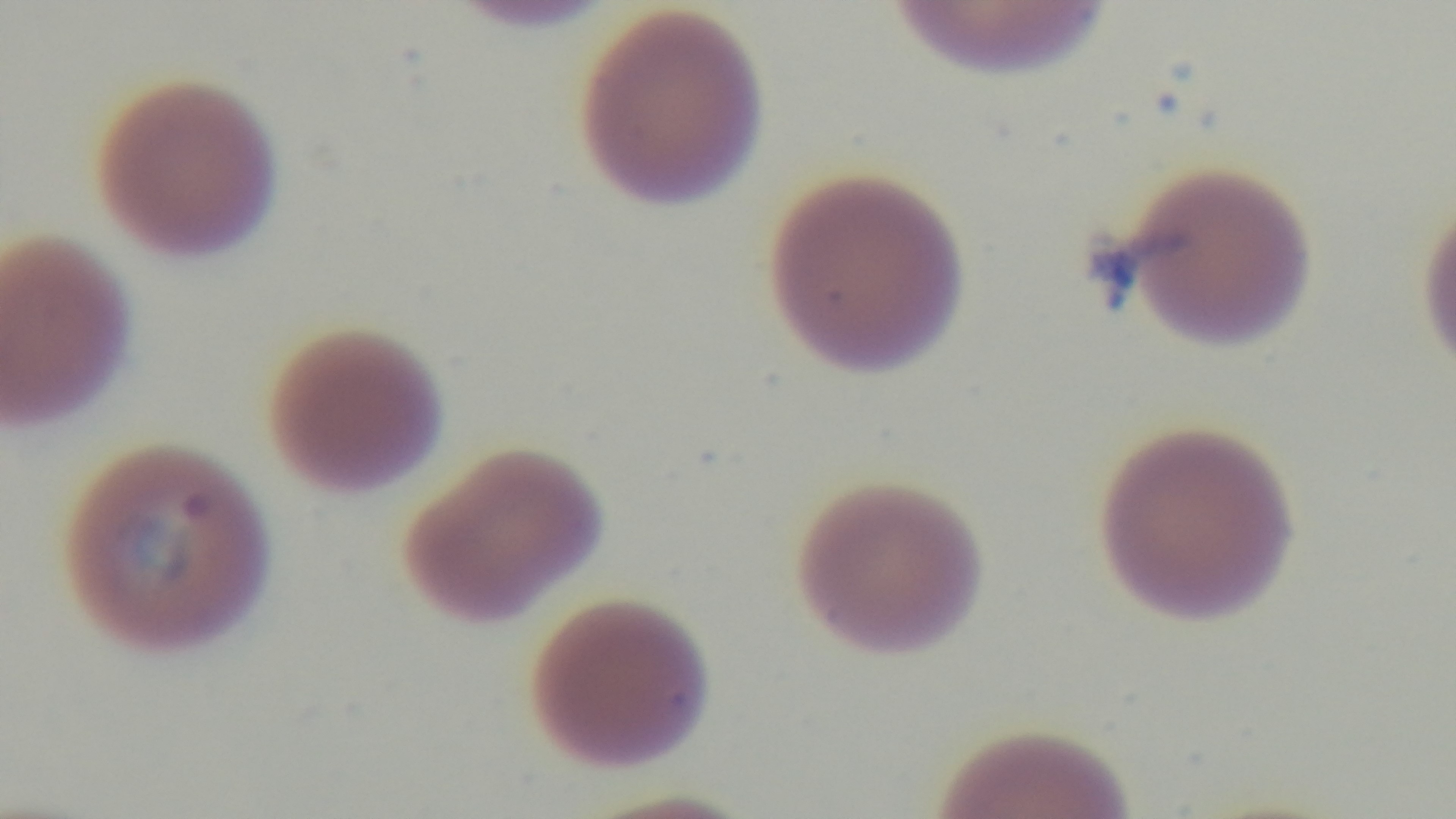
capture = mounted 4K digital camera
malaria status = positive
modality = light microscopy
objective = 100x oil immersion
stain = Giemsa
field of view = single
preparation = thin